Report the malaria status of this cell.
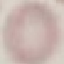
Uninfected.

capture: smartphone through the microscope eyepiece
image_type: automatically extracted cell patch, resized to 64 × 64 pixels
preparation: thin blood film
stain: Giemsa